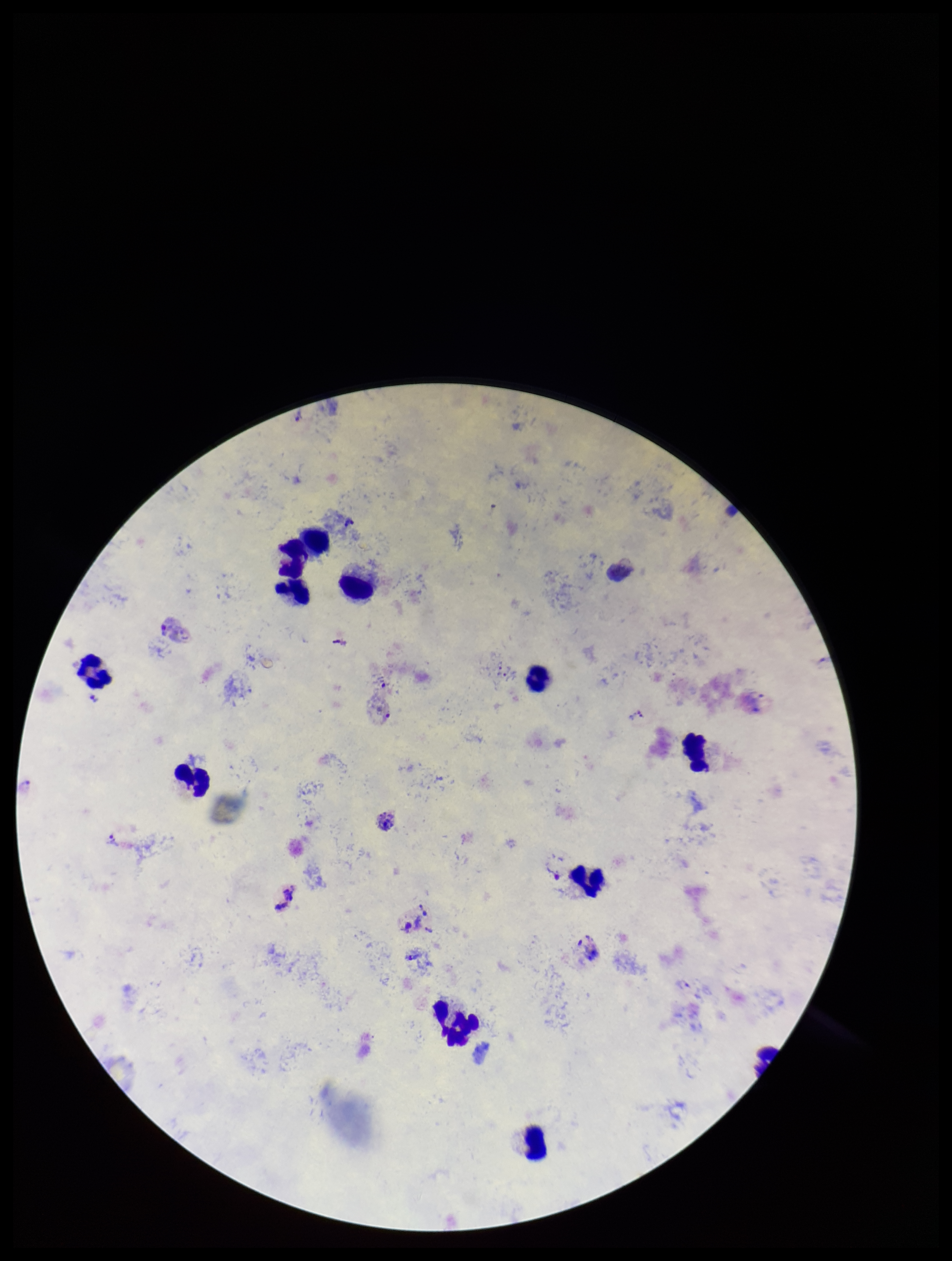
field of view = one from this slide
species reported for this patient = Plasmodium vivax
capture = smartphone photograph through the microscope eyepiece
preparation = thick smear
stain = Giemsa
parasite count = 3
leukocyte count = 10
image size = 952×1261 pixels
patient malaria status = positive
Plasmodium parasites = detected